State the blood parasite species.
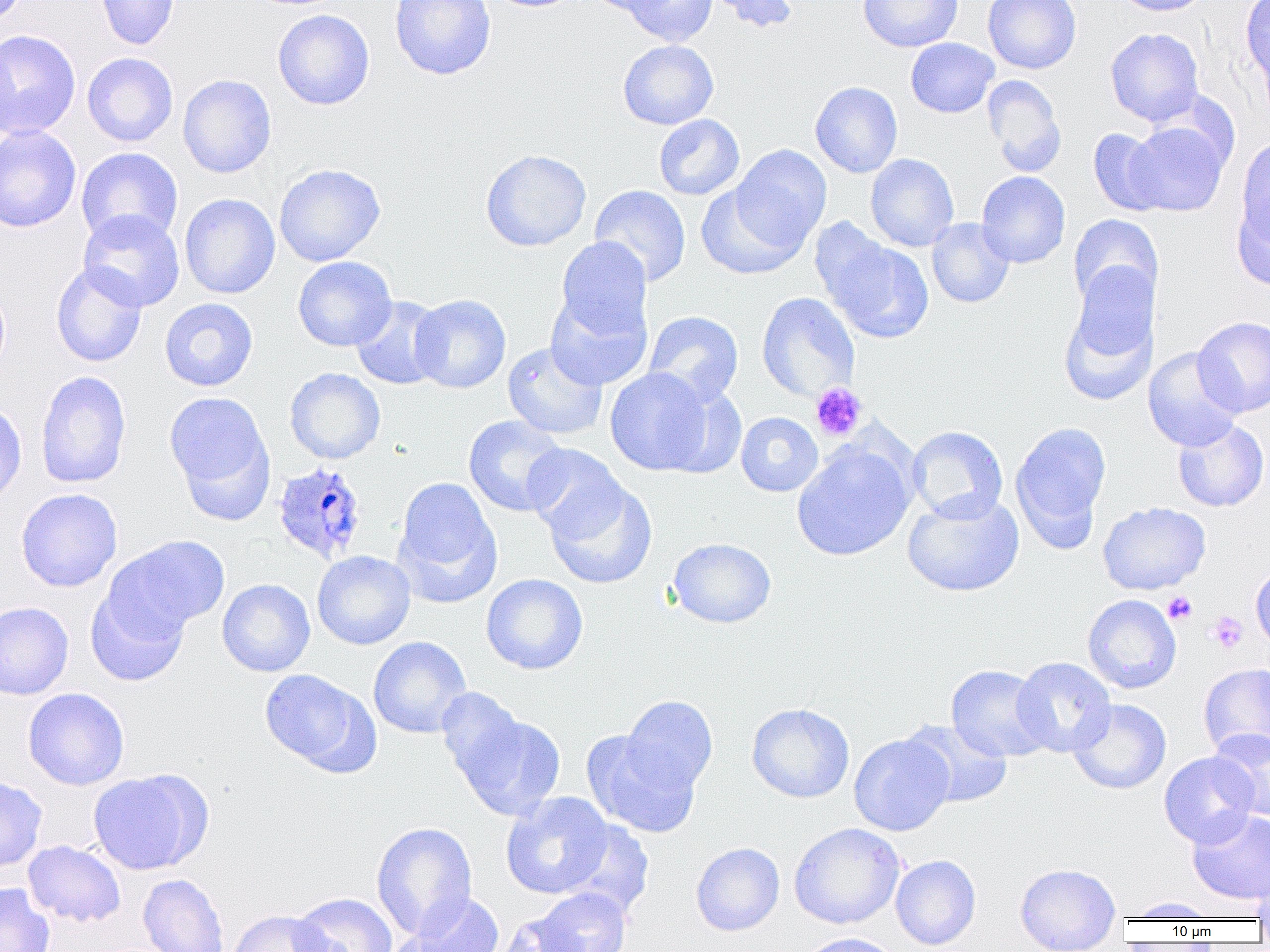

Plasmodium ovale.

Summary:
  - Coordinate format: approximate bounding boxes as named x1/y1/x2/y2 corners in pixels
  - Platelet locations: (x1=810, y1=382, x2=866, y2=441), (x1=1162, y1=592, x2=1197, y2=625), (x1=1207, y1=611, x2=1248, y2=654)
  - Plasmodium ovale-infected red blood cell locations: (x1=271, y1=461, x2=369, y2=564)
  - Uninfected red blood cell locations: (x1=0, y1=0, x2=30, y2=27), (x1=96, y1=0, x2=180, y2=50), (x1=389, y1=0, x2=496, y2=80), (x1=582, y1=0, x2=674, y2=16), (x1=620, y1=0, x2=718, y2=46), (x1=709, y1=0, x2=798, y2=33), (x1=858, y1=0, x2=963, y2=52), (x1=983, y1=0, x2=1082, y2=74), (x1=1112, y1=0, x2=1214, y2=16), (x1=1241, y1=0, x2=1269, y2=90), (x1=273, y1=9, x2=375, y2=110), (x1=1105, y1=27, x2=1204, y2=126), (x1=0, y1=30, x2=81, y2=139), (x1=905, y1=37, x2=999, y2=118), (x1=0, y1=39, x2=18, y2=143), (x1=618, y1=39, x2=718, y2=129), (x1=82, y1=52, x2=178, y2=147), (x1=178, y1=74, x2=277, y2=178), (x1=983, y1=75, x2=1067, y2=177), (x1=810, y1=82, x2=903, y2=178), (x1=654, y1=114, x2=744, y2=200), (x1=1123, y1=120, x2=1231, y2=216), (x1=0, y1=125, x2=81, y2=232), (x1=1088, y1=128, x2=1169, y2=216), (x1=1236, y1=135, x2=1270, y2=253), (x1=731, y1=145, x2=832, y2=251), (x1=76, y1=147, x2=183, y2=245), (x1=480, y1=149, x2=591, y2=251), (x1=866, y1=153, x2=959, y2=252), (x1=274, y1=163, x2=385, y2=267), (x1=976, y1=171, x2=1070, y2=268), (x1=696, y1=182, x2=806, y2=280), (x1=589, y1=184, x2=691, y2=287), (x1=1232, y1=190, x2=1270, y2=291), (x1=179, y1=194, x2=280, y2=299), (x1=77, y1=210, x2=185, y2=311), (x1=1068, y1=214, x2=1163, y2=312), (x1=927, y1=218, x2=1015, y2=308), (x1=819, y1=233, x2=935, y2=344), (x1=555, y1=238, x2=651, y2=342), (x1=293, y1=256, x2=397, y2=351), (x1=51, y1=262, x2=147, y2=368), (x1=0, y1=282, x2=10, y2=378), (x1=1059, y1=286, x2=1156, y2=407), (x1=545, y1=289, x2=652, y2=390), (x1=757, y1=292, x2=860, y2=401), (x1=409, y1=294, x2=511, y2=394), (x1=350, y1=296, x2=447, y2=390), (x1=159, y1=298, x2=258, y2=391), (x1=644, y1=311, x2=743, y2=407), (x1=1192, y1=316, x2=1270, y2=418), (x1=502, y1=341, x2=608, y2=440), (x1=1143, y1=347, x2=1244, y2=452), (x1=605, y1=367, x2=716, y2=476), (x1=284, y1=368, x2=386, y2=464), (x1=35, y1=370, x2=132, y2=489), (x1=164, y1=391, x2=273, y2=509), (x1=0, y1=401, x2=27, y2=509), (x1=736, y1=412, x2=823, y2=496), (x1=463, y1=415, x2=569, y2=517), (x1=1172, y1=418, x2=1269, y2=512), (x1=1010, y1=421, x2=1111, y2=547), (x1=907, y1=425, x2=1007, y2=523), (x1=792, y1=443, x2=914, y2=561), (x1=522, y1=444, x2=628, y2=541), (x1=542, y1=476, x2=657, y2=590), (x1=394, y1=477, x2=501, y2=604), (x1=15, y1=488, x2=123, y2=592), (x1=902, y1=491, x2=1024, y2=597), (x1=1098, y1=502, x2=1211, y2=595), (x1=106, y1=535, x2=229, y2=638), (x1=668, y1=537, x2=777, y2=628), (x1=312, y1=550, x2=416, y2=650), (x1=1250, y1=561, x2=1270, y2=651), (x1=481, y1=573, x2=588, y2=675), (x1=217, y1=579, x2=315, y2=677), (x1=85, y1=586, x2=190, y2=686), (x1=1082, y1=594, x2=1182, y2=693), (x1=0, y1=602, x2=74, y2=699), (x1=368, y1=636, x2=472, y2=739), (x1=1011, y1=657, x2=1116, y2=757), (x1=1198, y1=663, x2=1270, y2=760), (x1=946, y1=664, x2=1053, y2=763), (x1=258, y1=669, x2=375, y2=773), (x1=436, y1=686, x2=529, y2=788), (x1=22, y1=688, x2=129, y2=790), (x1=621, y1=695, x2=718, y2=794), (x1=1068, y1=698, x2=1171, y2=794), (x1=746, y1=703, x2=855, y2=803), (x1=452, y1=708, x2=566, y2=821), (x1=901, y1=719, x2=1013, y2=808), (x1=1209, y1=729, x2=1270, y2=822), (x1=581, y1=731, x2=701, y2=838), (x1=849, y1=733, x2=954, y2=836), (x1=1159, y1=751, x2=1260, y2=848), (x1=87, y1=770, x2=207, y2=875), (x1=0, y1=776, x2=47, y2=872), (x1=500, y1=792, x2=615, y2=899), (x1=1187, y1=809, x2=1270, y2=905), (x1=559, y1=819, x2=654, y2=917), (x1=371, y1=821, x2=477, y2=940), (x1=789, y1=822, x2=905, y2=929), (x1=23, y1=840, x2=126, y2=927), (x1=691, y1=842, x2=785, y2=936), (x1=891, y1=855, x2=981, y2=950), (x1=1251, y1=862, x2=1270, y2=927), (x1=1015, y1=863, x2=1120, y2=952), (x1=138, y1=874, x2=229, y2=952), (x1=0, y1=883, x2=55, y2=952), (x1=533, y1=887, x2=632, y2=952), (x1=290, y1=892, x2=398, y2=952), (x1=397, y1=892, x2=505, y2=952), (x1=1126, y1=897, x2=1220, y2=921), (x1=226, y1=908, x2=335, y2=952), (x1=496, y1=912, x2=589, y2=952), (x1=798, y1=933, x2=902, y2=952)
  - Field of view: one of a larger specimen
  - Modality: light microscopy
  - Preparation: thin blood smear
  - Magnification: 1000x
  - Image size: 1270×952 pixels